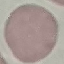
Result: no malaria parasites seen. Acquired by smartphone through the microscope eyepiece. Giemsa-stained preparation. Thin smear of blood. Automatically extracted cell patch, resized to 64 × 64 pixels.